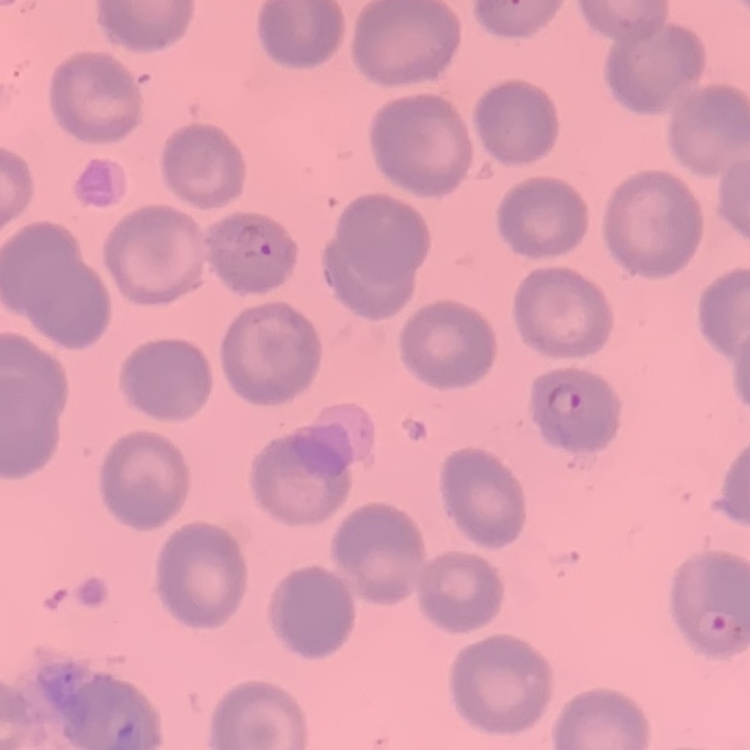
{
  "erythrocyte_morphology": "no rouleaux formation",
  "stain": "Field's or Giemsa",
  "preparation": "thin peripheral smear",
  "image_type": "one tile cut from a larger photomicrograph"
}